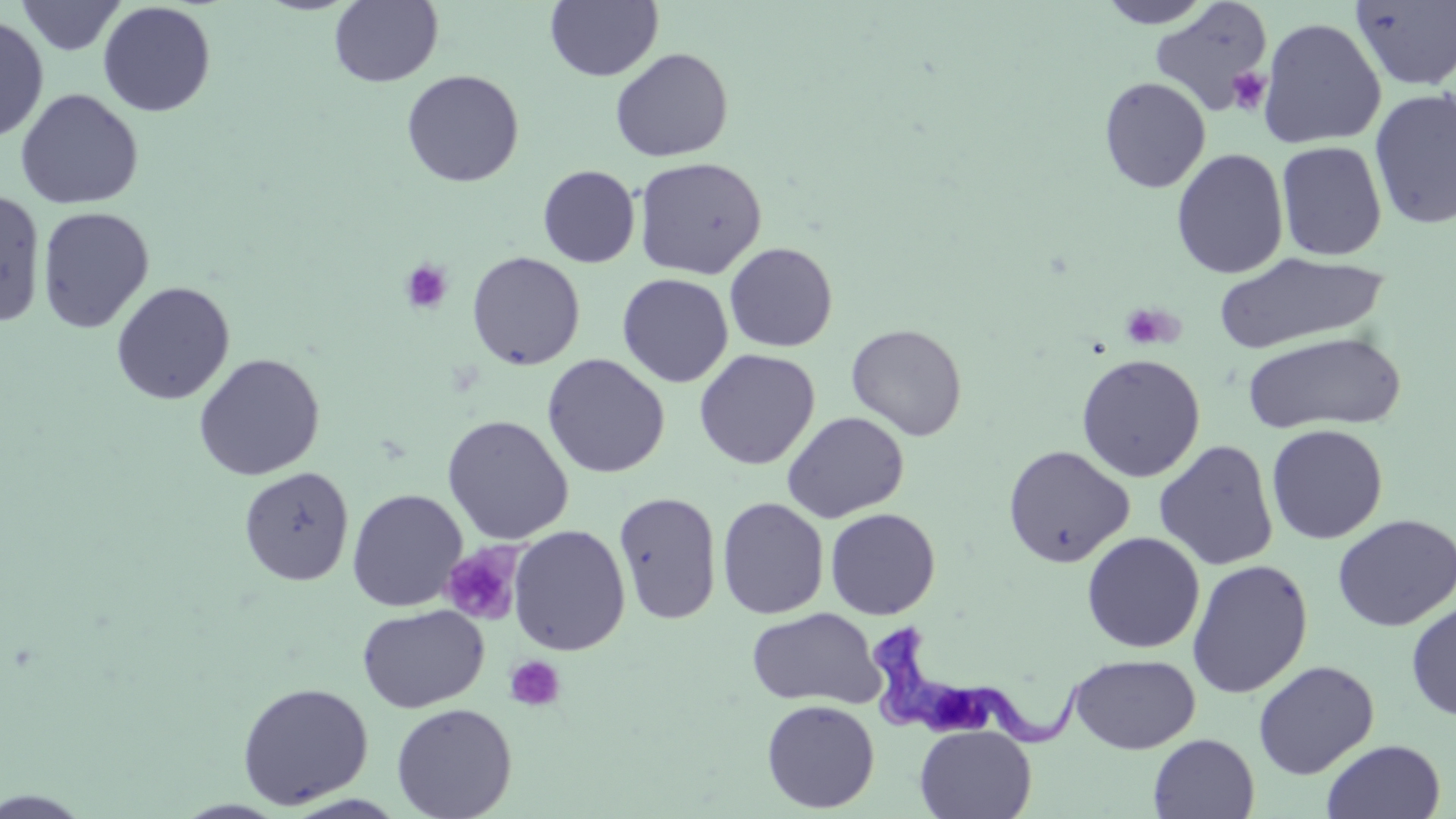
slide-level diagnosis = Trypanosoma brucei
uninfected red blood cell locations = approximate bounding boxes as named x1/y1/x2/y2 corners in pixels: (x1=15, y1=0, x2=128, y2=56), (x1=329, y1=0, x2=443, y2=87), (x1=1095, y1=0, x2=1217, y2=29), (x1=545, y1=1, x2=663, y2=82), (x1=1350, y1=1, x2=1456, y2=91), (x1=97, y1=2, x2=217, y2=117), (x1=1149, y1=2, x2=1274, y2=118), (x1=0, y1=15, x2=49, y2=144), (x1=1258, y1=17, x2=1386, y2=149), (x1=610, y1=47, x2=733, y2=162), (x1=401, y1=69, x2=524, y2=187), (x1=1098, y1=76, x2=1212, y2=194), (x1=1369, y1=87, x2=1456, y2=231), (x1=15, y1=88, x2=143, y2=209), (x1=1276, y1=141, x2=1388, y2=261), (x1=1171, y1=148, x2=1289, y2=279), (x1=634, y1=156, x2=767, y2=280), (x1=537, y1=164, x2=640, y2=268), (x1=0, y1=190, x2=47, y2=328), (x1=37, y1=206, x2=155, y2=333), (x1=724, y1=242, x2=838, y2=352), (x1=467, y1=251, x2=585, y2=370), (x1=1213, y1=251, x2=1387, y2=354), (x1=617, y1=273, x2=734, y2=388), (x1=111, y1=281, x2=235, y2=405), (x1=845, y1=323, x2=967, y2=441), (x1=1242, y1=331, x2=1406, y2=434), (x1=694, y1=349, x2=820, y2=469), (x1=193, y1=353, x2=325, y2=481), (x1=542, y1=353, x2=670, y2=478), (x1=1076, y1=353, x2=1205, y2=482), (x1=782, y1=411, x2=909, y2=523), (x1=441, y1=414, x2=575, y2=544), (x1=1266, y1=423, x2=1388, y2=544), (x1=1154, y1=439, x2=1278, y2=571), (x1=1003, y1=444, x2=1135, y2=568), (x1=238, y1=466, x2=354, y2=586), (x1=347, y1=489, x2=467, y2=611), (x1=613, y1=490, x2=723, y2=625), (x1=716, y1=497, x2=829, y2=619), (x1=824, y1=508, x2=941, y2=620), (x1=1332, y1=514, x2=1456, y2=632), (x1=508, y1=525, x2=631, y2=656), (x1=1081, y1=532, x2=1205, y2=653), (x1=1187, y1=560, x2=1313, y2=698), (x1=1406, y1=598, x2=1456, y2=722), (x1=357, y1=604, x2=488, y2=713), (x1=747, y1=607, x2=885, y2=709), (x1=1069, y1=654, x2=1201, y2=754), (x1=1253, y1=660, x2=1379, y2=780), (x1=237, y1=681, x2=373, y2=809), (x1=761, y1=699, x2=880, y2=813), (x1=391, y1=702, x2=517, y2=819), (x1=914, y1=724, x2=1036, y2=819), (x1=1148, y1=734, x2=1259, y2=819), (x1=1322, y1=739, x2=1446, y2=819), (x1=1, y1=788, x2=96, y2=818), (x1=172, y1=799, x2=290, y2=818)
stain = May-Grünwald-Giemsa
preparation = thin blood film
modality = optical microscopy
platelet locations = approximate bounding boxes as named x1/y1/x2/y2 corners in pixels: (x1=1228, y1=67, x2=1271, y2=114), (x1=400, y1=259, x2=453, y2=314), (x1=1121, y1=302, x2=1180, y2=351), (x1=440, y1=546, x2=522, y2=625), (x1=504, y1=655, x2=565, y2=711)
image size = 1456×819 pixels
magnification = 1000x
Trypanosoma brucei locations = approximate bounding boxes as named x1/y1/x2/y2 corners in pixels: (x1=866, y1=621, x2=1091, y2=750)
field of view = single